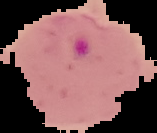

malaria_status: parasitized
preparation: thin blood smear
image_type: segmented cell region with the area outside set to black
image_size: 157×133 pixels